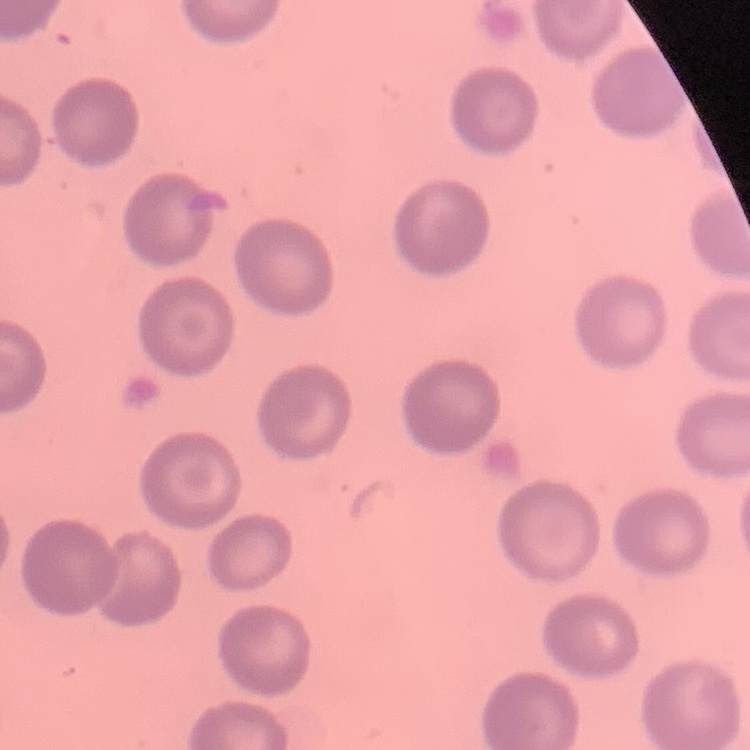
The red blood cells exhibit no rouleaux formation. Thin blood film. Field's or Giemsa stain. One tile cut from a larger photomicrograph.